Locate and identify every blood parasite.
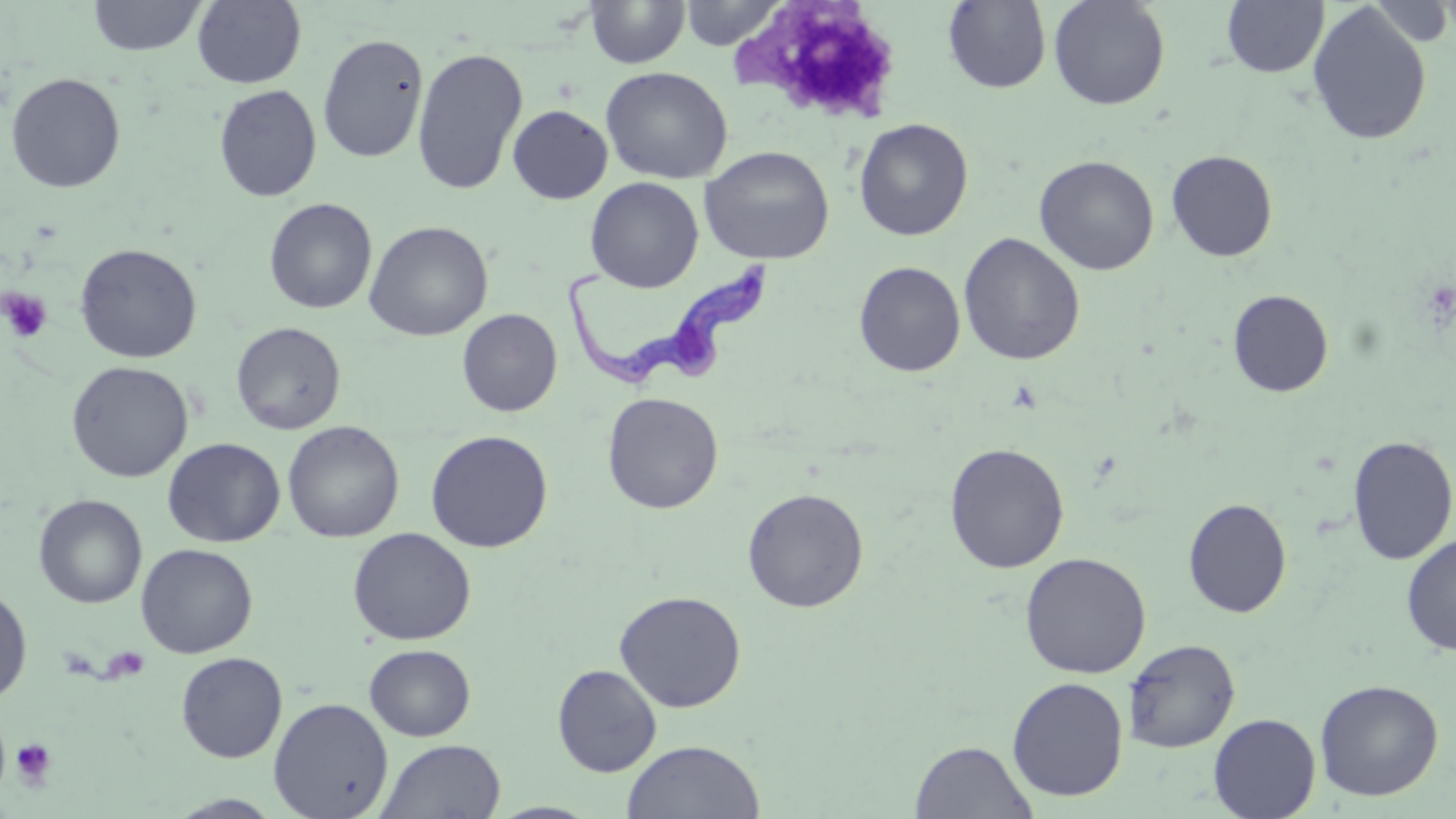
Approximate bounding boxes as [x1, y1, x2, y2] in pixels.
Trypanosoma brucei: [565, 267, 778, 394].
No Plasmodium falciparum, Plasmodium ovale, Plasmodium malariae, Plasmodium vivax, or Babesia divergens observed.

Uninfected red blood cell locations: [87, 0, 209, 57], [191, 0, 307, 88], [679, 0, 787, 49], [1048, 0, 1170, 110], [584, 1, 690, 69], [943, 1, 1052, 93], [1221, 1, 1329, 79], [1307, 3, 1432, 146], [317, 32, 429, 163], [411, 47, 528, 196], [600, 66, 733, 184], [5, 72, 126, 194], [213, 84, 322, 202], [507, 104, 613, 204], [853, 118, 974, 241], [699, 145, 835, 265], [1166, 149, 1278, 261], [1034, 155, 1160, 275], [585, 177, 704, 292], [264, 197, 377, 314], [364, 221, 493, 342], [958, 232, 1085, 365], [74, 243, 202, 363], [854, 261, 966, 377], [1228, 289, 1333, 397], [457, 308, 562, 417], [231, 321, 347, 435], [66, 361, 193, 482], [602, 392, 724, 514], [282, 421, 404, 543], [425, 429, 553, 553], [1347, 435, 1456, 565], [162, 437, 285, 547], [944, 442, 1070, 573], [742, 487, 869, 613], [33, 494, 147, 609], [1182, 498, 1292, 618], [347, 527, 476, 645], [1401, 533, 1456, 655], [136, 543, 257, 658], [1019, 552, 1152, 678], [0, 585, 33, 705], [614, 590, 747, 712], [1122, 638, 1240, 753], [364, 644, 476, 741], [175, 652, 287, 763], [552, 664, 662, 777], [1007, 676, 1129, 802], [1314, 679, 1444, 801], [268, 697, 393, 818], [1208, 713, 1320, 819], [375, 738, 506, 819], [621, 739, 765, 819], [910, 740, 1038, 819], [166, 794, 286, 818], [486, 802, 603, 818]. Platelet locations: [1, 288, 53, 343], [11, 738, 57, 787]. Slide-level diagnosis: Trypanosoma brucei. Thin blood smear. Captured at 1000x magnification. May-Grünwald-Giemsa-stained preparation. Single field of view. Optical microscopy. Image is 1456×819 pixels.